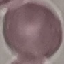

result = negative for malaria parasites
stain = Giemsa
image type = automatically extracted cell patch, resized to 64 × 64 pixels
preparation = thin smear
capture = smartphone through the microscope eyepiece